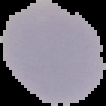

Malaria status: uninfected. Cell region segmented out of the field of view; the surrounding area is masked to black. Image is 106×106 pixels. From a thin blood film.